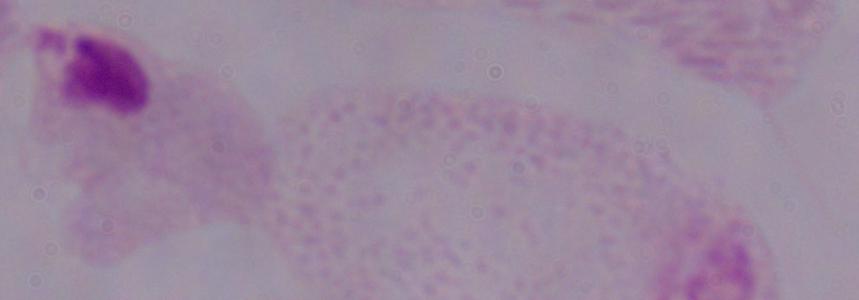

Summary:
  - Magnification: 1000x
  - Identification: trichomonad
  - Modality: photomicrograph